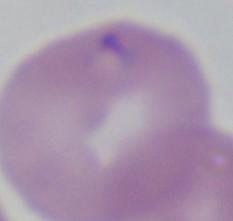

A Babesia parasite is seen. Captured at 1000x magnification. Micrograph.